Assess the morphology of the red blood cells.
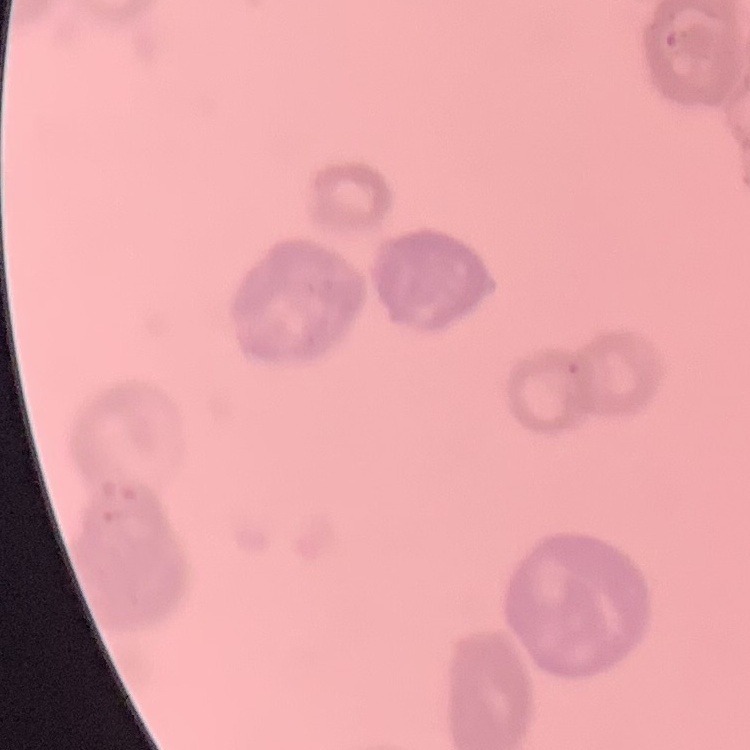

They show rouleaux formation.

Thin blood film. Square crop of a larger photomicrograph. Field's or Giemsa stain.